Report the malaria status of this cell.
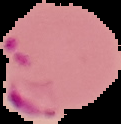

Parasitized.

Image is 121×124 pixels. The area outside the segmented cell region is set to black. From a thin blood smear.